Locate every malaria parasite.
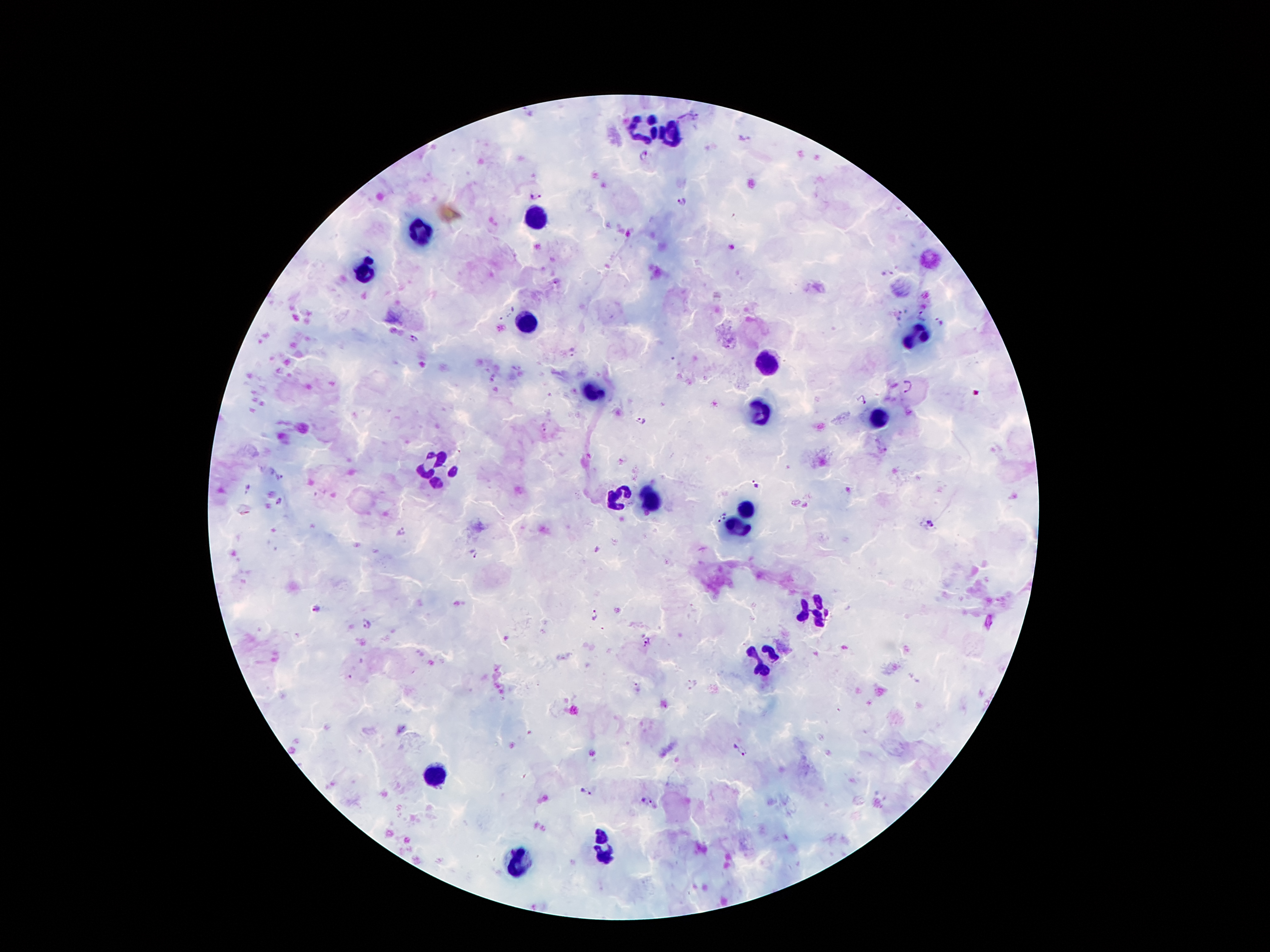
Approximate object centers, in pixels from the top-left corner.
Malaria parasites: (x=745, y=137), (x=643, y=153), (x=537, y=193), (x=681, y=201), (x=509, y=312), (x=921, y=314), (x=938, y=321), (x=415, y=340), (x=573, y=351), (x=908, y=386), (x=861, y=397), (x=642, y=420), (x=544, y=427), (x=282, y=479), (x=754, y=483), (x=246, y=489), (x=279, y=502), (x=726, y=515), (x=718, y=519), (x=931, y=523), (x=402, y=532), (x=597, y=551), (x=474, y=554), (x=318, y=606), (x=594, y=614), (x=366, y=624), (x=648, y=643), (x=695, y=685), (x=637, y=688), (x=739, y=750), (x=587, y=792), (x=647, y=800).

Summary:
  - Leukocyte locations: (x=643, y=129), (x=671, y=140), (x=536, y=218), (x=421, y=232), (x=365, y=271), (x=524, y=319), (x=914, y=337), (x=765, y=362), (x=594, y=390), (x=762, y=410), (x=878, y=420), (x=429, y=460), (x=443, y=480), (x=616, y=496), (x=650, y=498), (x=744, y=510), (x=738, y=525), (x=814, y=611), (x=765, y=659), (x=434, y=773), (x=602, y=849), (x=522, y=859)
  - Patient malaria status: positive for Plasmodium falciparum
  - Capture: smartphone through the microscope eyepiece
  - Image size: 1270×952 pixels
  - Field of view: single
  - Magnification: 100x
  - Preparation: thick peripheral-blood smear
  - Stain: Giemsa